Give the position of every P. falciparum parasite, noting its life-cycle stage.
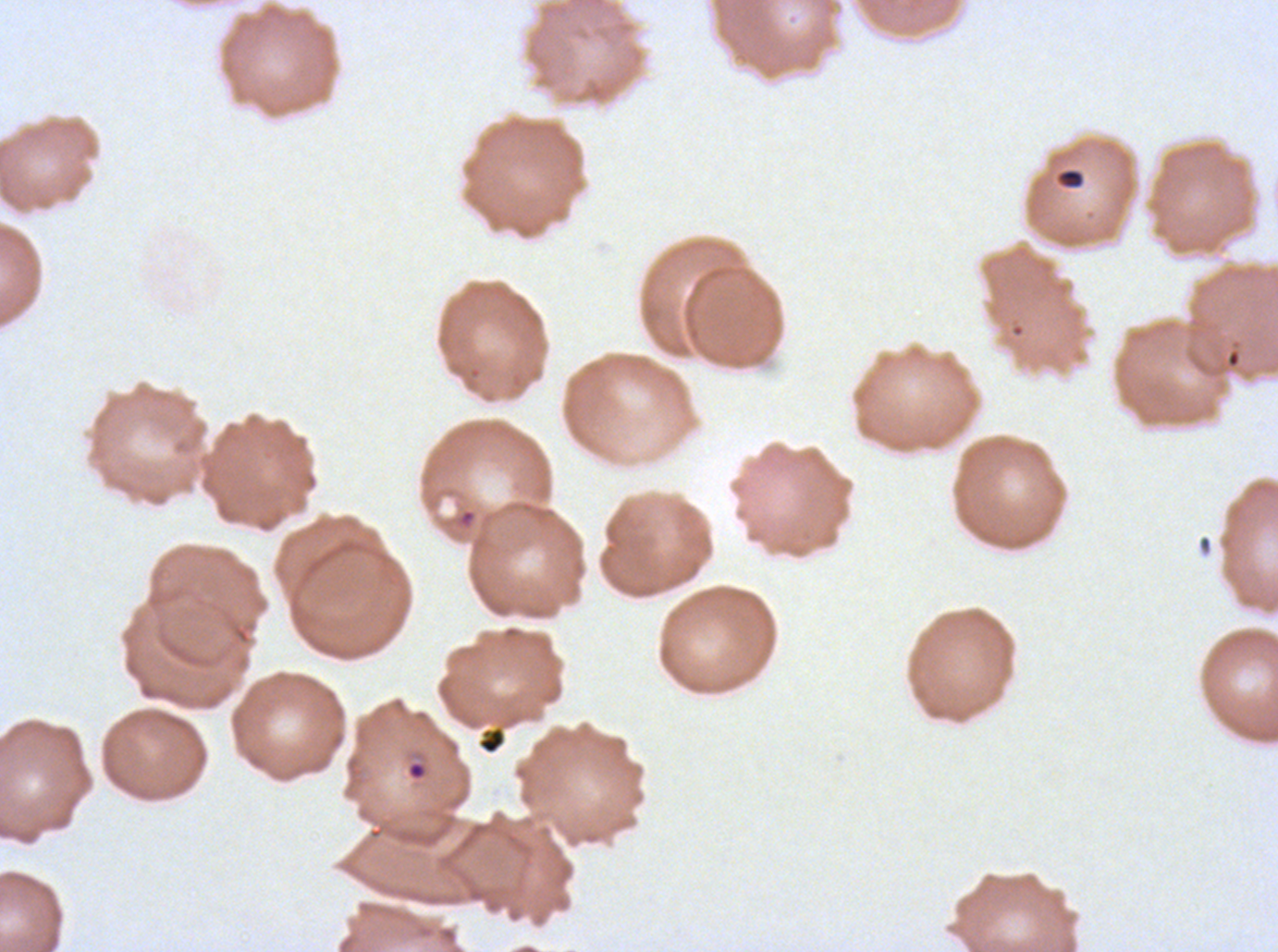

Approximate bounding boxes as (x1, y1, x2, y2) in pixels.
Rings: (458, 508, 476, 528).
No late-ring/early-trophozoite forms, mid trophozoites, late trophozoites, early schizonts, late schizonts, segmenters, or gametocytes observed.

Debris locations: (1056, 167, 1085, 189), (476, 726, 507, 755). Ex-vivo P. falciparum culture from a patient in The Gambia, grown for 24 to 48 hours. A sub-image separated from a larger composite. Giemsa-stained preparation. Thin blood film. Image is 1278×952 pixels.